Report the malaria status of this cell.
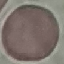

Uninfected.

Giemsa stain. Automatically extracted cell patch, resized to 64 × 64 pixels. Photographed with a smartphone camera at the microscope eyepiece. Thin smear of blood.